Assess the morphology of the erythrocytes.
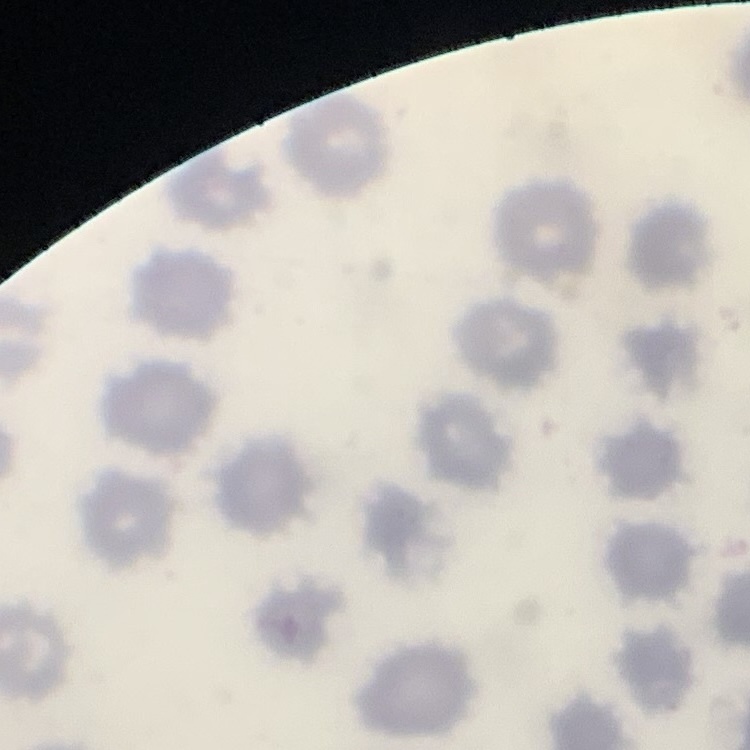
No rouleaux formation.

Summary:
  - Preparation: thin blood film
  - Image type: one tile cut from a larger photomicrograph
  - Stain: Field's or Giemsa